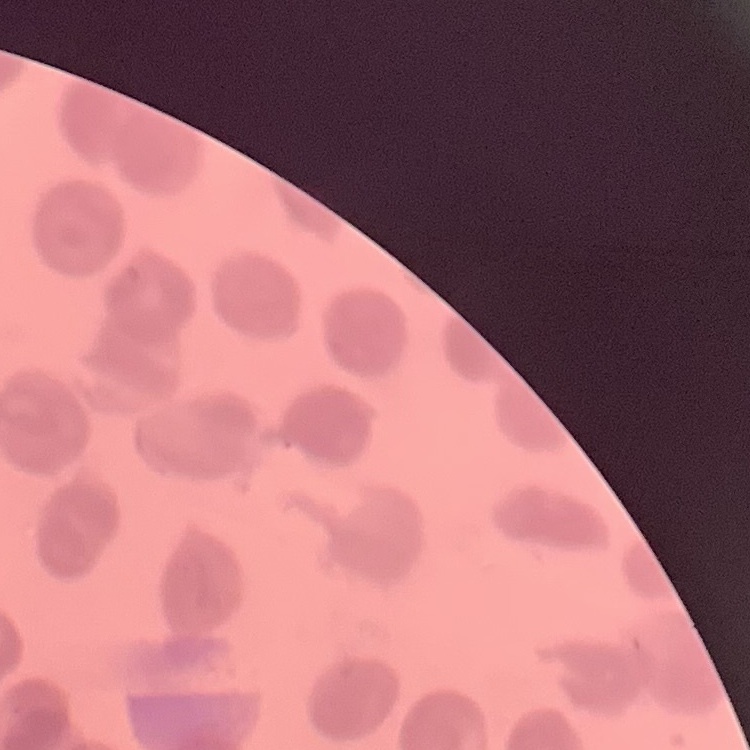
Summary:
  - Erythrocyte morphology: no rouleaux formation
  - Stain: Field's or Giemsa
  - Image type: one tile cut from a larger photomicrograph
  - Preparation: thin blood smear